Point out each leukocyte.
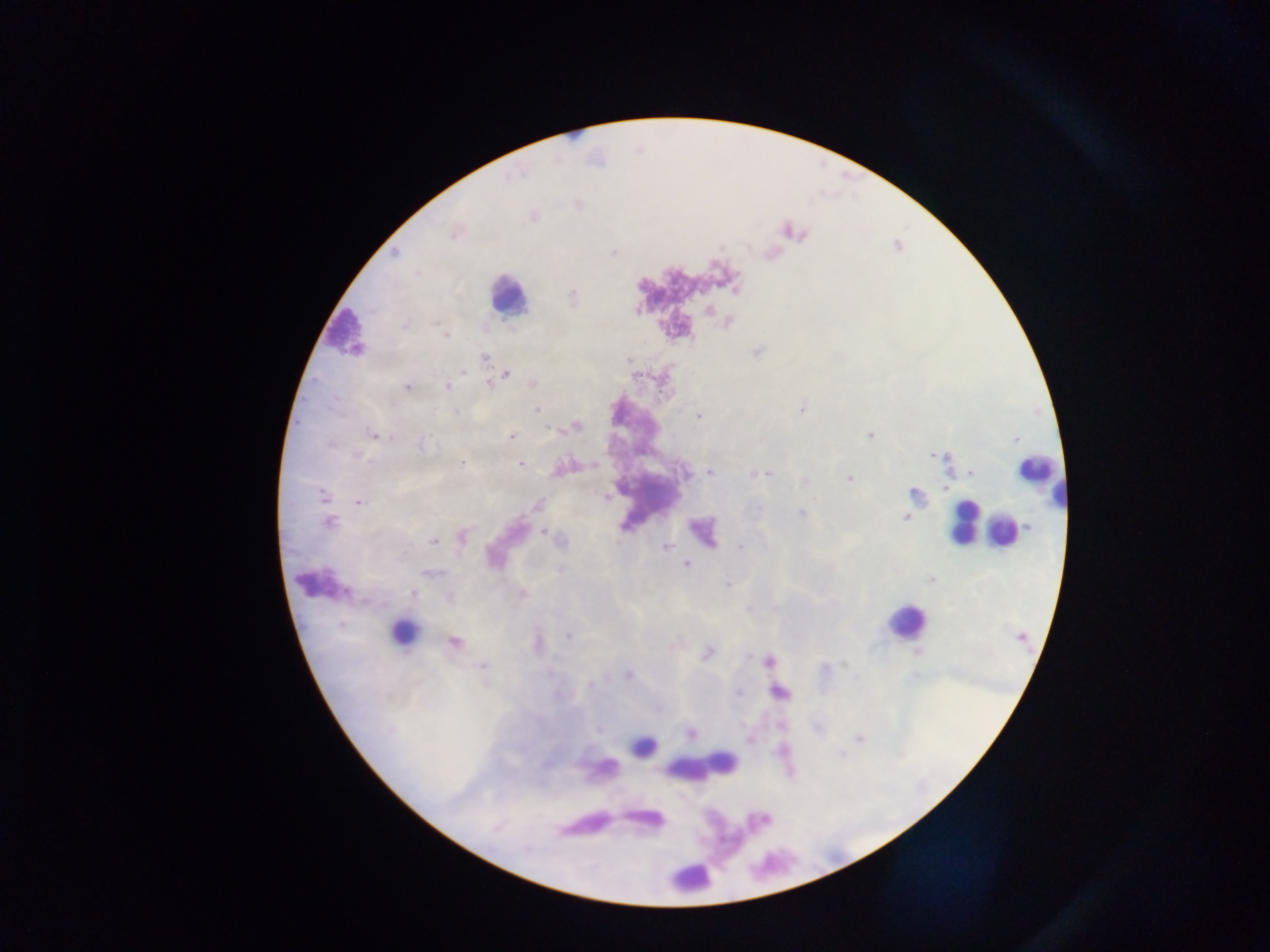
Approximate centers as {x, y} in pixels.
Leukocytes: {508, 296}, {346, 331}, {1036, 476}, {963, 522}, {1002, 531}, {906, 621}, {403, 631}, {644, 745}, {722, 762}, {692, 873}.

image_size: 1270×952 pixels
plasmodium_parasite_locations: 'approximate centers as {x, y} in pixels: {394, 253}, {613, 253}, {572, 295}, {708, 310}, {405, 325}, {445, 335}, {757, 351}, {485, 357}, {463, 372}, {507, 375}, {488, 383}, {533, 384}, {407, 387}, {448, 387}, {801, 409}, {538, 410}, {433, 412}, {456, 412}, {698, 415}, {577, 427}, {374, 434}, {870, 434}, {510, 437}, {1016, 439}, {330, 444}, {422, 444}, {932, 455}, {359, 457}, {462, 463}, {520, 464}, {683, 472}, {710, 472}, {972, 473}, {754, 474}, {767, 474}, {849, 478}, {805, 481}, {915, 494}, {323, 495}, {606, 497}, {358, 502}, {537, 505}, {757, 508}, {801, 514}, {906, 517}, {329, 523}, {623, 528}, {543, 532}, {463, 537}, {434, 540}, {666, 547}, {740, 547}, {686, 564}, {561, 569}, {434, 572}, {931, 579}, {728, 584}, {413, 593}, {522, 593}, {450, 597}, {569, 636}, {454, 641}, {707, 654}, {767, 660}, {483, 666}, {825, 667}, {628, 674}, {590, 685}, {739, 692}, {691, 733}, {748, 738}, {859, 738}'
country: Ghana
field_of_view: single
preparation: thick blood smear
capture: mobile-phone photograph through a microscope